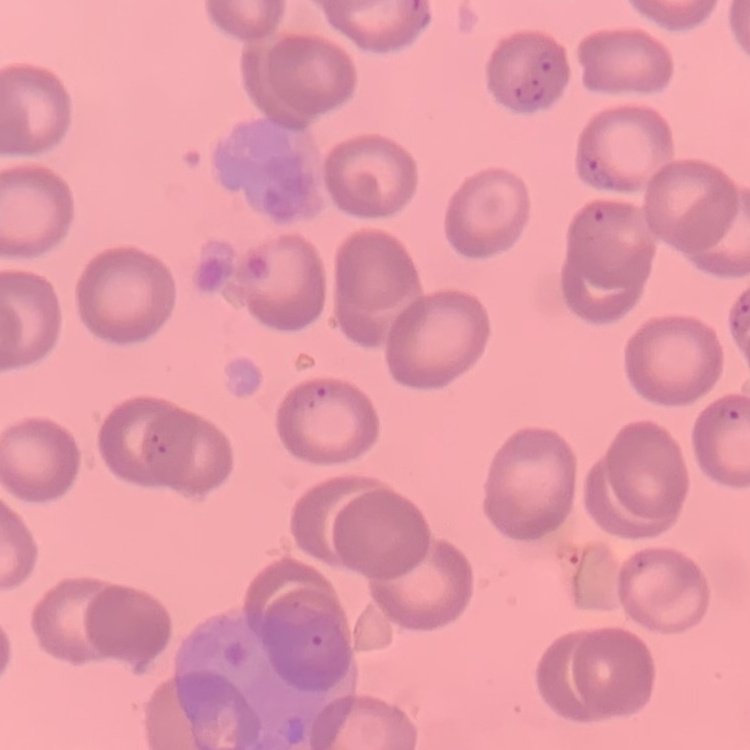

{
  "red_blood_cell_morphology": "no rouleaux formation",
  "preparation": "thin blood film",
  "stain": "Field's or Giemsa",
  "image_type": "one tile cut from a larger photomicrograph"
}